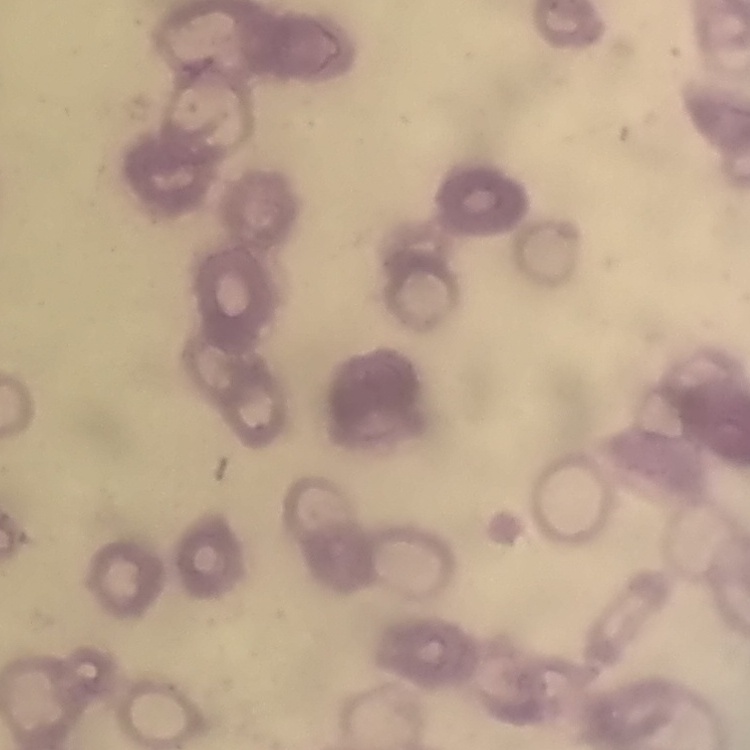
{
  "erythrocyte_morphology": "rouleaux formation",
  "image_type": "one tile cut from a larger photomicrograph",
  "stain": "Field's or Giemsa",
  "preparation": "thin peripheral smear"
}